Give the position of every Plasmodium parasite.
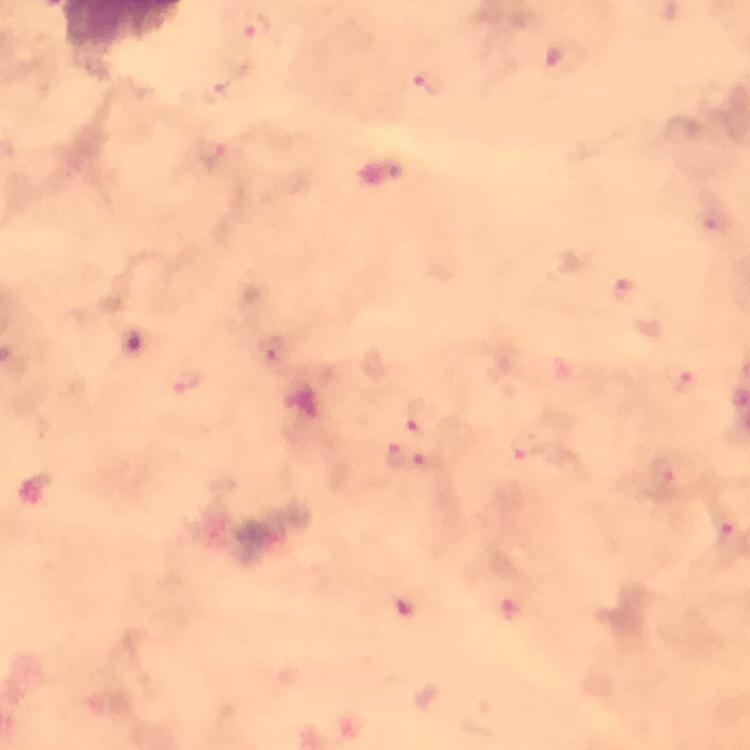

Approximate centers as (x, y) in pixels.
Plasmodium parasites: (256, 25), (429, 83), (213, 154), (718, 222), (622, 288), (271, 354), (678, 377), (187, 380), (414, 416), (528, 448), (394, 456), (430, 463), (665, 477), (726, 534), (404, 606), (511, 610).

Summary:
  - Image size: 750×750 pixels
  - Immersion oil: applied
  - Stain: Giemsa
  - Preparation: thick blood smear
  - Magnification: 100x
  - Capture: smartphone mounted on the microscope
  - Cropped from: a single field of view
  - Context: from a diagnostic examination for malaria